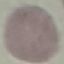

Result: no malaria parasites detected. Giemsa stain. Thin blood smear. Photographed with a smartphone camera at the microscope eyepiece. Automatically extracted cell patch, resized to 64 × 64 pixels.